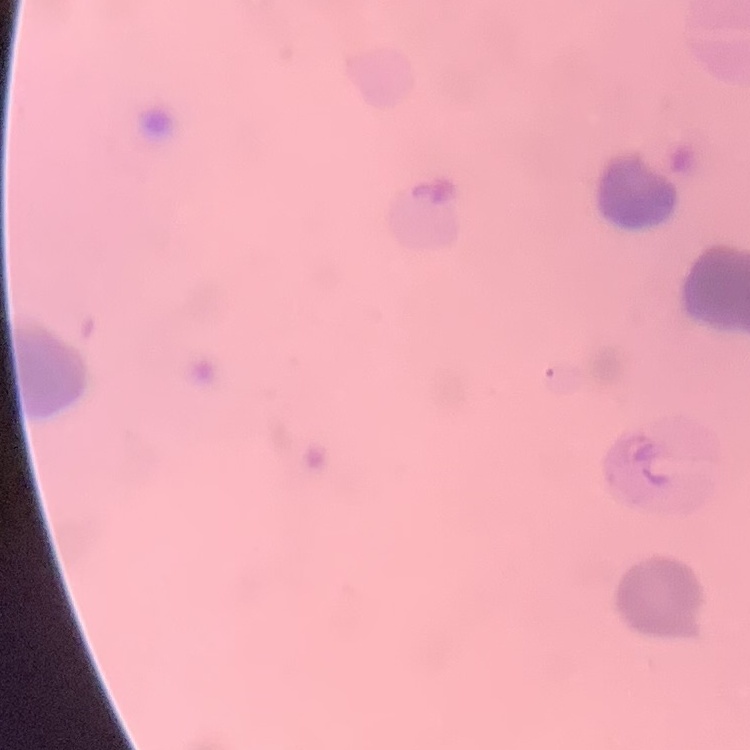
red blood cell morphology = rouleaux formation
image type = one tile cut from a larger photomicrograph
stain = Field's or Giemsa
preparation = thin blood smear